Name the parasite shown.
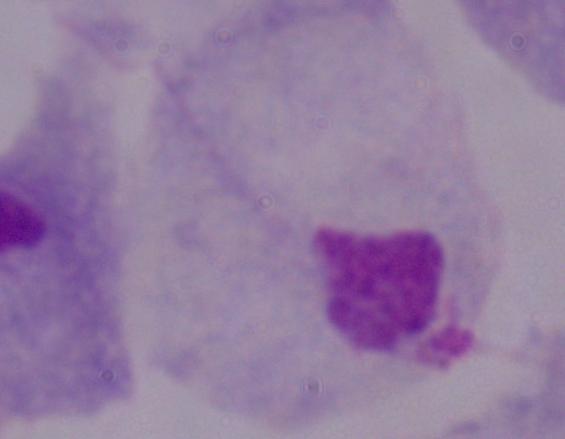

This is a trichomonad.

Captured at 1000x magnification. Photomicrograph.